State which parasite is depicted.
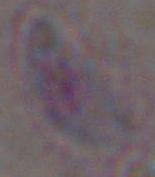

Toxoplasma gondii.

Summary:
  - Modality: micrograph
  - Magnification: 1000x